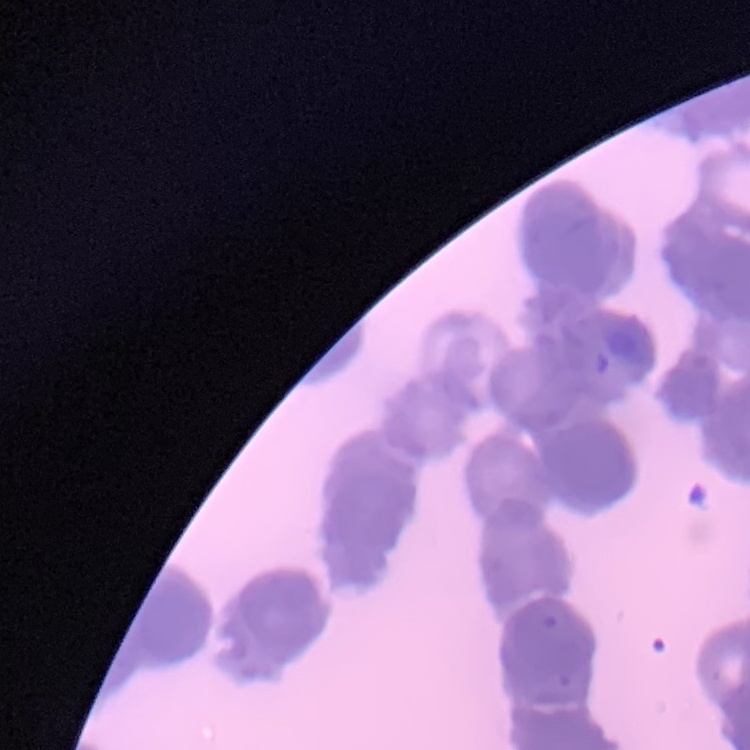

red blood cell morphology = rouleaux formation
preparation = thin blood smear
stain = Field's or Giemsa
image type = square crop of a larger photomicrograph